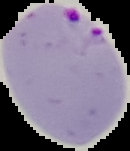

From a thin blood film. Result: Plasmodium parasites detected. The area outside the segmented cell region is set to black. Image is 130×151 pixels.